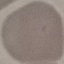 Malaria status: uninfected. Acquired by smartphone through the microscope eyepiece. Giemsa stain. Automatically extracted cell patch, resized to 64 × 64 pixels. Thin blood film.